Identify the preparation type.
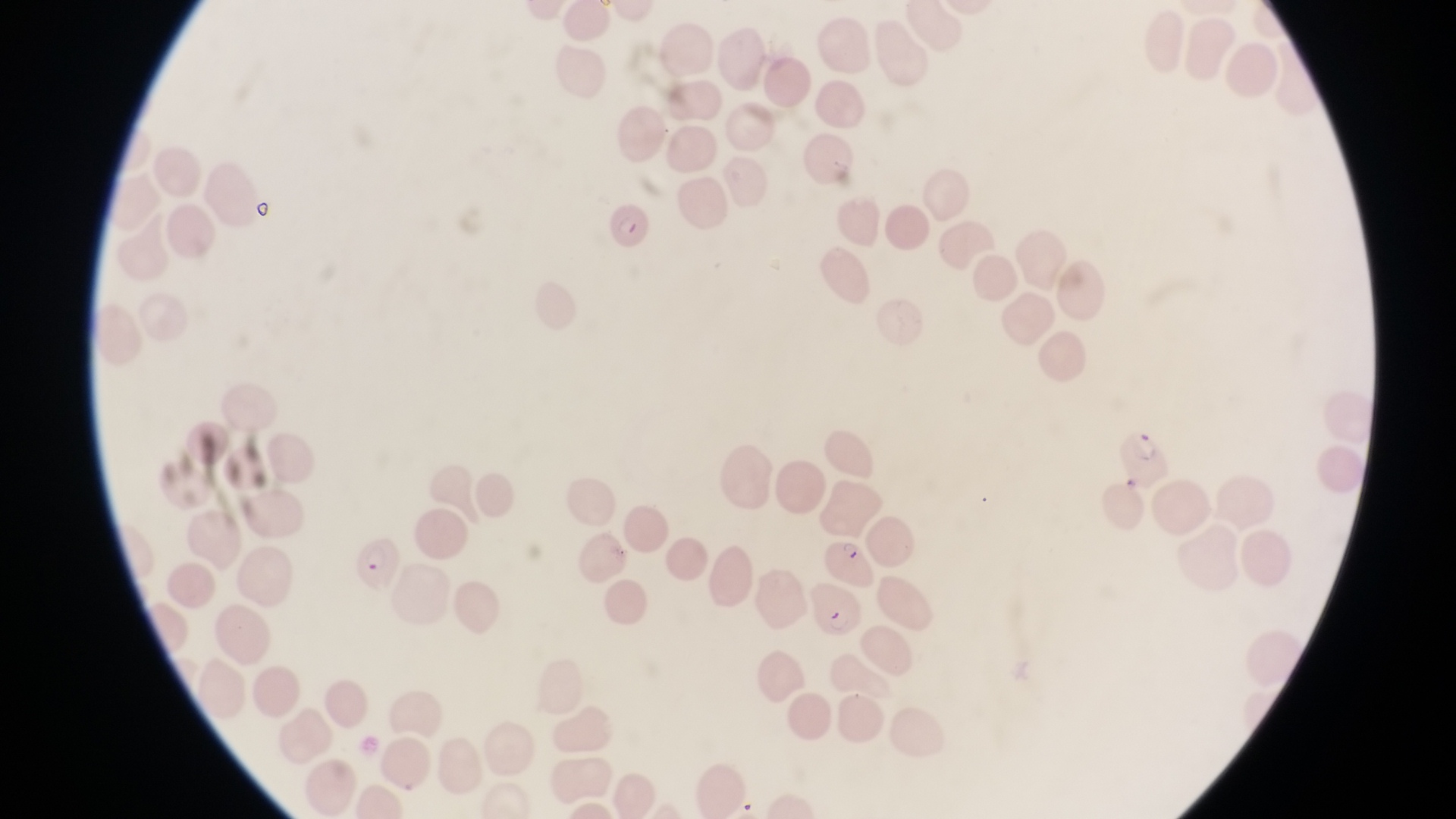
Thin blood smear.

country = Uganda
capture = smartphone photograph through the eyepiece of an Olympus CX-23 microscope
field of view = single
magnification = 1000x
image size = 1456×819 pixels
parasitised red blood cell locations = approximate bounding boxes as {left, top, right, bottom} in pixels: {602, 199, 655, 252}, {1122, 422, 1171, 489}, {824, 531, 884, 595}, {347, 534, 405, 594}, {806, 581, 862, 640}